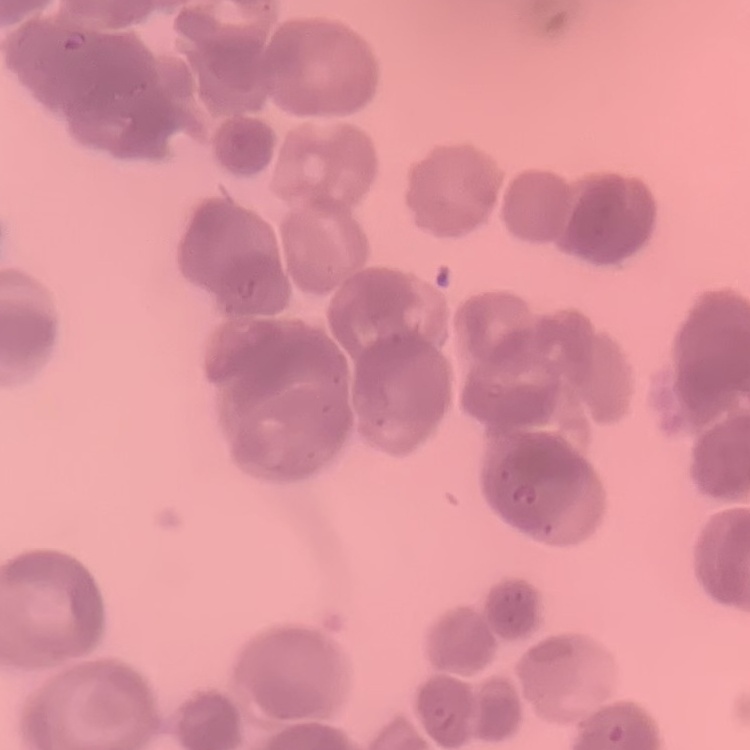

The erythrocytes show rouleaux formation. One tile cut from a larger photomicrograph. Thin peripheral smear. Stained with either Field's or Giemsa.